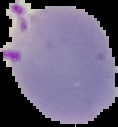

{
  "image_type": "segmented cell region with the area outside set to black",
  "malaria_status": "parasitized",
  "preparation": "thin blood smear",
  "image_size": "118×127 pixels"
}